Identify the cell.
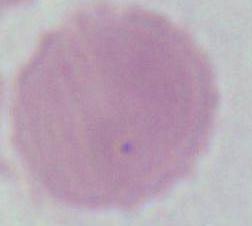
An erythrocyte.

Captured at 1000x magnification. Micrograph.